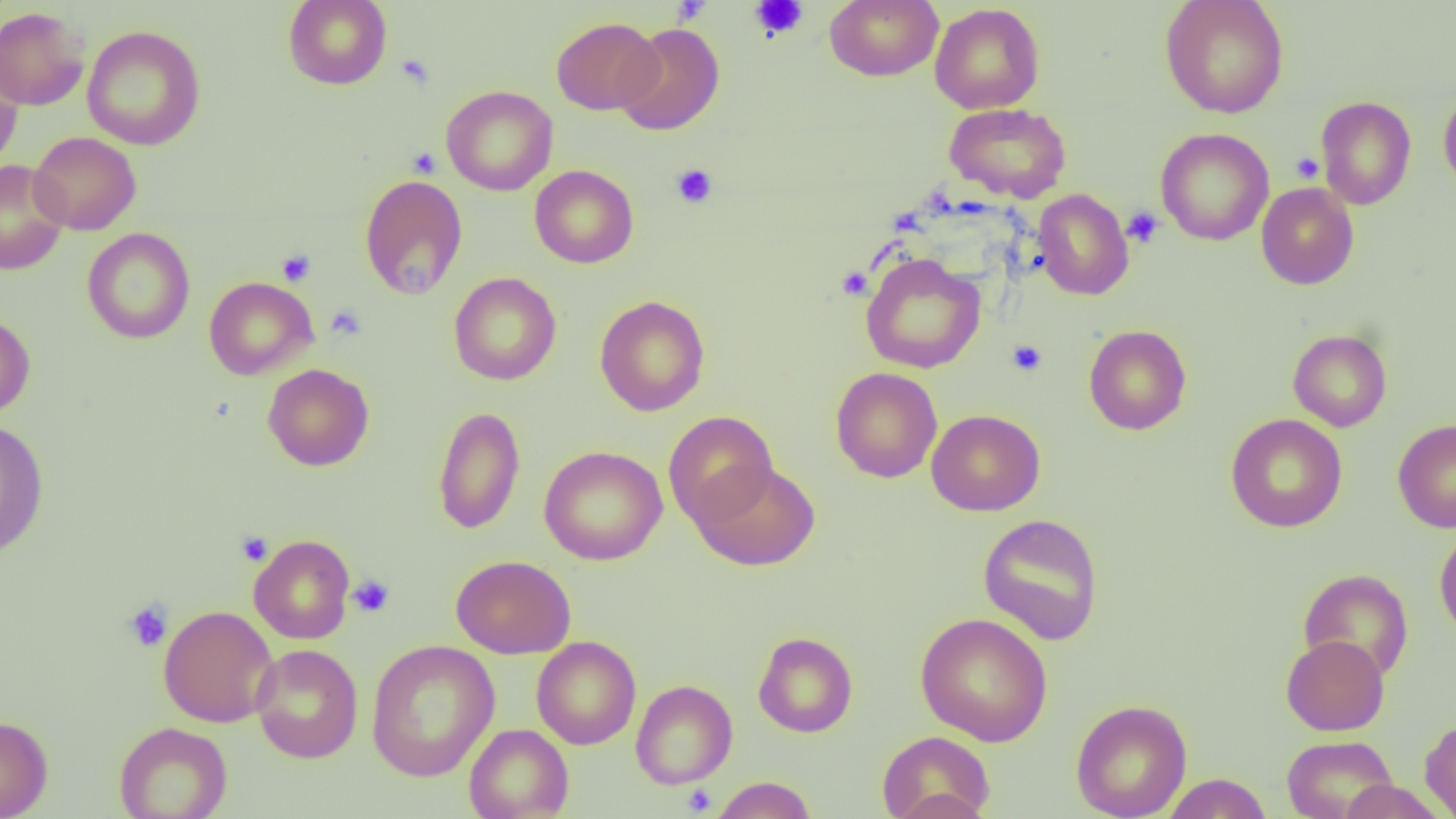
slide-level diagnosis = no evidence of blood parasites
platelet locations = approximate bounding boxes as (x1, y1, x2, y2) in pixels: (750, 0, 808, 40), (396, 54, 434, 89), (407, 147, 441, 178), (1290, 152, 1324, 183), (670, 163, 718, 208), (1122, 206, 1164, 248), (276, 249, 316, 286), (836, 266, 872, 300), (325, 305, 365, 340), (1006, 340, 1048, 376), (236, 532, 272, 566), (347, 574, 395, 617), (123, 601, 173, 652), (680, 784, 717, 815)
preparation = thin blood film
image size = 1456×819 pixels
magnification = 1000x
field of view = one of a larger specimen
modality = optical microscopy
uninfected red blood cell locations = approximate bounding boxes as (x1, y1, x2, y2) in pixels: (282, 0, 392, 90), (824, 0, 943, 81), (1159, 0, 1289, 118), (929, 3, 1045, 114), (0, 6, 89, 111), (551, 17, 664, 115), (615, 22, 725, 136), (83, 25, 206, 151), (0, 57, 23, 175), (441, 85, 557, 196), (1438, 86, 1456, 196), (1315, 96, 1417, 210), (944, 103, 1071, 202), (1156, 127, 1274, 245), (29, 131, 141, 235), (0, 160, 69, 275), (529, 165, 638, 268), (359, 174, 468, 300), (1256, 182, 1359, 290), (1033, 189, 1133, 301), (82, 228, 195, 344), (860, 252, 986, 374), (448, 272, 561, 386), (204, 276, 318, 380), (594, 295, 710, 416), (0, 309, 35, 418), (1083, 325, 1192, 435), (1288, 329, 1392, 432), (262, 364, 374, 471), (831, 367, 942, 483), (432, 405, 525, 535), (926, 409, 1045, 516), (663, 410, 778, 530), (1225, 413, 1347, 533), (0, 417, 49, 558), (1393, 419, 1456, 533), (539, 445, 667, 565), (691, 461, 820, 571), (978, 513, 1104, 645), (1434, 527, 1456, 645), (248, 534, 355, 644), (451, 555, 576, 658), (1298, 568, 1414, 682), (158, 604, 279, 727), (915, 612, 1053, 746), (753, 631, 858, 737), (1281, 635, 1389, 735), (531, 636, 641, 749), (366, 639, 500, 782), (250, 643, 364, 763), (630, 679, 738, 789), (1070, 699, 1192, 819), (0, 715, 53, 819), (1420, 716, 1456, 817), (113, 722, 232, 819), (463, 724, 574, 818), (877, 730, 996, 819), (1281, 735, 1399, 819), (1161, 773, 1273, 818), (710, 776, 817, 819), (1337, 779, 1446, 818), (883, 787, 993, 819)